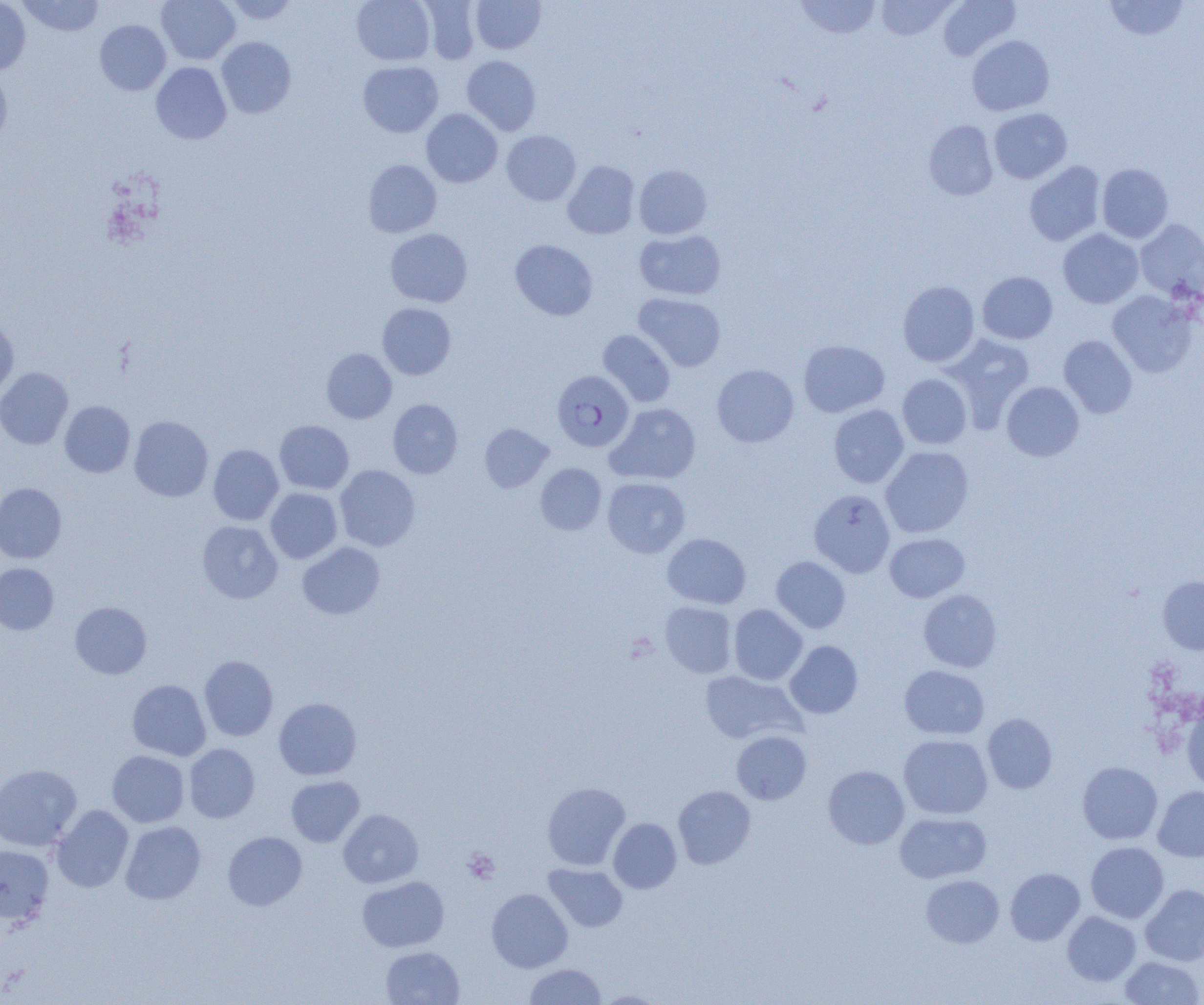

Approximate bounding boxes as (x1,y1)-(x2,y2) corner pairs in pixels. Plasmodium falciparum-infected red blood cell locations: (552,370)-(633,451). Platelet locations: (463,848)-(499,884). Uninfected red blood cell locations: (17,0)-(104,36), (157,0)-(240,64), (224,0)-(300,24), (352,0)-(435,65), (794,0)-(881,40), (875,0)-(956,41), (938,0)-(1020,61), (0,1)-(31,75), (419,1)-(481,64), (471,1)-(545,53), (1104,1)-(1190,41), (94,20)-(170,95), (967,35)-(1054,116), (216,37)-(296,118), (462,55)-(541,135), (358,61)-(443,137), (151,62)-(232,144), (0,69)-(12,147), (988,107)-(1071,184), (421,109)-(502,187), (923,120)-(999,201), (501,131)-(580,205), (363,159)-(441,237), (563,161)-(639,239), (1024,161)-(1105,246), (1097,163)-(1173,243), (634,164)-(712,239), (1135,219)-(1204,302), (385,228)-(472,307), (1058,228)-(1144,309), (635,229)-(725,300), (510,239)-(597,321), (978,271)-(1058,344), (898,281)-(980,366), (1107,290)-(1198,378), (634,293)-(726,371), (377,302)-(456,380), (0,319)-(18,400), (598,330)-(676,406), (940,333)-(1035,430), (1058,335)-(1137,418), (798,339)-(890,418), (322,348)-(396,423), (712,364)-(799,447), (0,367)-(73,449), (897,374)-(972,449), (1001,381)-(1084,461), (388,399)-(462,478), (60,401)-(135,477), (606,403)-(700,484), (828,404)-(909,488), (129,416)-(213,501), (274,420)-(353,494), (480,423)-(553,492), (208,444)-(283,525), (881,446)-(973,537), (535,463)-(606,535), (334,465)-(420,551), (602,477)-(690,558), (0,483)-(66,563), (266,488)-(342,563), (808,489)-(895,578), (197,521)-(282,603), (662,533)-(751,609), (885,533)-(969,602), (297,542)-(384,619), (771,556)-(851,633), (0,563)-(58,634), (1158,575)-(1204,655), (918,589)-(1002,672), (660,601)-(738,678), (70,602)-(152,678), (728,604)-(807,685), (784,641)-(863,719), (199,655)-(278,741), (898,665)-(989,740), (699,670)-(805,744), (127,679)-(211,761), (274,697)-(361,780), (1182,699)-(1204,793), (982,713)-(1057,794), (731,731)-(811,804), (898,734)-(993,820), (184,743)-(260,823), (107,750)-(189,827), (1077,762)-(1162,844), (0,764)-(81,851), (823,765)-(909,849), (286,776)-(364,847), (542,782)-(630,871), (673,785)-(756,869), (1153,786)-(1204,861), (52,805)-(134,892), (338,809)-(423,888), (894,812)-(991,884), (608,817)-(682,893), (120,821)-(206,905), (223,831)-(307,910), (1086,842)-(1169,923), (0,844)-(54,925), (543,863)-(627,932), (1005,868)-(1085,945), (921,874)-(1004,948), (357,876)-(449,952), (1140,884)-(1204,966), (486,888)-(573,972), (1062,911)-(1141,985), (381,946)-(464,1004), (1119,955)-(1203,1005), (524,963)-(606,1005), (594,989)-(669,1004). Slide-level diagnosis: Plasmodium falciparum. Captured at 1000x magnification. Thin blood film. One field of a larger specimen. Image is 1204×1005 pixels. Optical microscopy.